State which cell type is depicted.
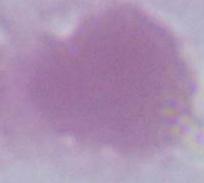
This is an erythrocyte.

1000x magnification. Photomicrograph.